Locate and identify every blood parasite.
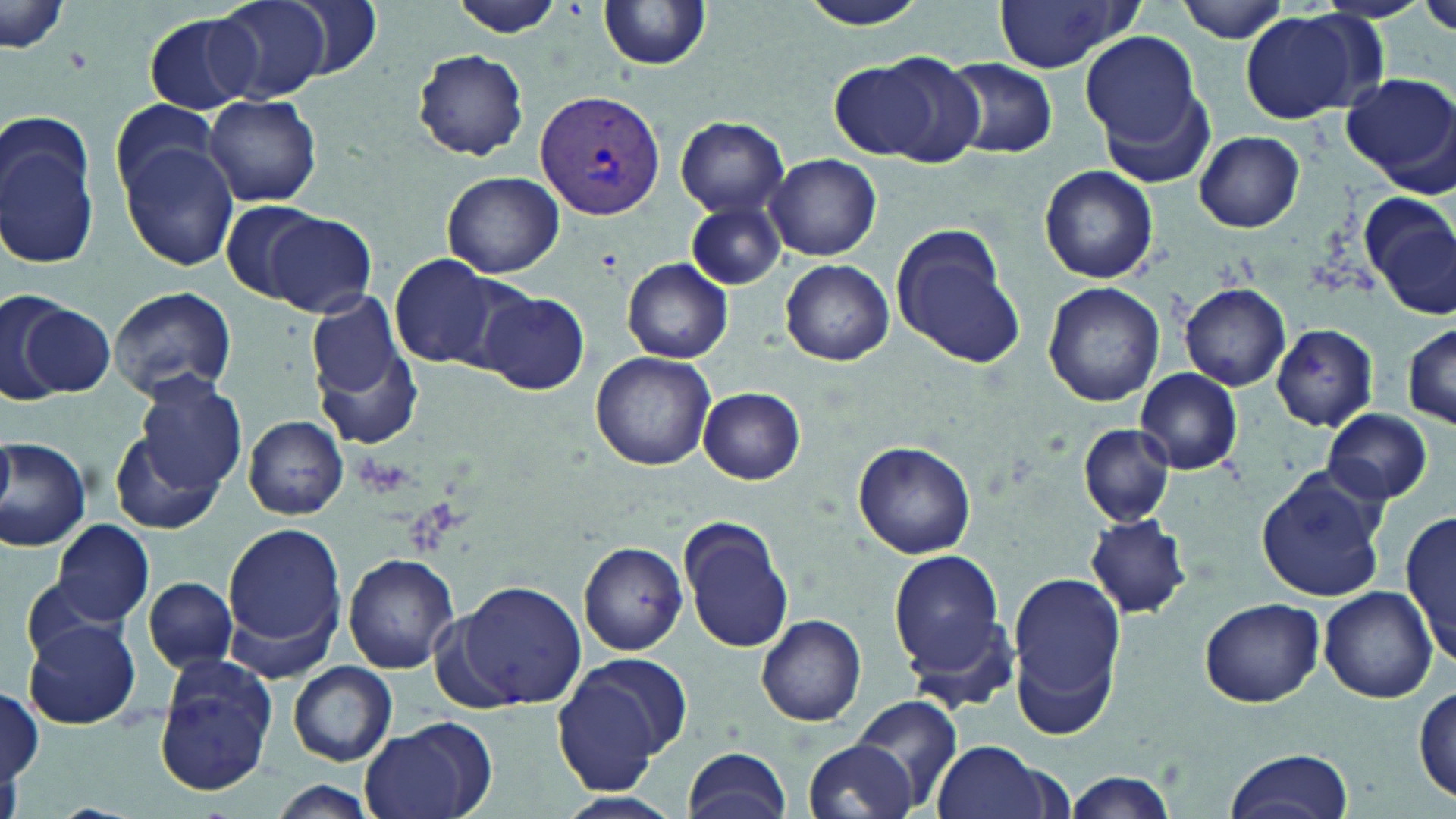
Approximate bounding boxes as named x1/y1/x2/y2 corners in pixels.
Plasmodium vivax-infected red blood cells: (x1=535, y1=89, x2=664, y2=219).
No Plasmodium falciparum, Plasmodium ovale, Plasmodium malariae, Babesia divergens, or Trypanosoma brucei observed.

slide-level diagnosis = Plasmodium vivax
stain = May-Grünwald-Giemsa
image size = 1456×819 pixels
magnification = 1000x
uninfected red blood cell locations = approximate bounding boxes as named x1/y1/x2/y2 corners in pixels: (x1=213, y1=0, x2=331, y2=102), (x1=287, y1=0, x2=387, y2=84), (x1=447, y1=0, x2=568, y2=36), (x1=798, y1=0, x2=930, y2=30), (x1=1173, y1=0, x2=1293, y2=43), (x1=1420, y1=0, x2=1456, y2=39), (x1=990, y1=1, x2=1139, y2=73), (x1=599, y1=2, x2=711, y2=72), (x1=1, y1=3, x2=71, y2=58), (x1=1239, y1=11, x2=1374, y2=125), (x1=143, y1=12, x2=261, y2=114), (x1=1080, y1=34, x2=1204, y2=156), (x1=414, y1=49, x2=530, y2=160), (x1=862, y1=52, x2=988, y2=165), (x1=944, y1=58, x2=1058, y2=159), (x1=832, y1=61, x2=935, y2=158), (x1=1096, y1=72, x2=1219, y2=190), (x1=1344, y1=73, x2=1456, y2=191), (x1=204, y1=95, x2=322, y2=206), (x1=110, y1=100, x2=221, y2=200), (x1=675, y1=115, x2=789, y2=215), (x1=0, y1=119, x2=100, y2=270), (x1=1194, y1=132, x2=1305, y2=232), (x1=120, y1=140, x2=239, y2=270), (x1=766, y1=153, x2=881, y2=260), (x1=1039, y1=166, x2=1158, y2=283), (x1=442, y1=171, x2=563, y2=278), (x1=1363, y1=196, x2=1456, y2=319), (x1=218, y1=199, x2=330, y2=304), (x1=685, y1=199, x2=785, y2=290), (x1=265, y1=213, x2=378, y2=317), (x1=888, y1=222, x2=1025, y2=371), (x1=390, y1=255, x2=500, y2=367), (x1=624, y1=258, x2=734, y2=362), (x1=782, y1=259, x2=894, y2=366), (x1=1042, y1=281, x2=1165, y2=407), (x1=1179, y1=283, x2=1291, y2=390), (x1=107, y1=286, x2=239, y2=403), (x1=1157, y1=288, x2=1276, y2=457), (x1=478, y1=290, x2=590, y2=395), (x1=1, y1=292, x2=104, y2=403), (x1=306, y1=294, x2=420, y2=448), (x1=1270, y1=322, x2=1380, y2=432), (x1=1404, y1=323, x2=1456, y2=429), (x1=591, y1=351, x2=717, y2=470), (x1=1135, y1=368, x2=1244, y2=475), (x1=130, y1=374, x2=249, y2=495), (x1=698, y1=387, x2=806, y2=485), (x1=1322, y1=408, x2=1434, y2=505), (x1=244, y1=416, x2=348, y2=519), (x1=1079, y1=424, x2=1174, y2=526), (x1=110, y1=433, x2=221, y2=535), (x1=1, y1=436, x2=93, y2=552), (x1=852, y1=441, x2=976, y2=560), (x1=1255, y1=470, x2=1388, y2=603), (x1=1401, y1=509, x2=1455, y2=662), (x1=1084, y1=513, x2=1191, y2=619), (x1=678, y1=516, x2=796, y2=653), (x1=51, y1=519, x2=155, y2=626), (x1=223, y1=521, x2=347, y2=660), (x1=578, y1=540, x2=688, y2=654), (x1=888, y1=547, x2=1015, y2=697), (x1=345, y1=553, x2=458, y2=674), (x1=1005, y1=567, x2=1127, y2=739), (x1=141, y1=577, x2=240, y2=674), (x1=453, y1=579, x2=586, y2=710), (x1=1318, y1=586, x2=1437, y2=702), (x1=1200, y1=598, x2=1324, y2=708), (x1=755, y1=614, x2=867, y2=727), (x1=23, y1=620, x2=142, y2=731), (x1=551, y1=655, x2=688, y2=793), (x1=154, y1=656, x2=280, y2=794), (x1=288, y1=660, x2=397, y2=766), (x1=1414, y1=687, x2=1455, y2=805), (x1=0, y1=689, x2=45, y2=784), (x1=845, y1=695, x2=966, y2=812), (x1=358, y1=716, x2=495, y2=819), (x1=804, y1=738, x2=918, y2=819), (x1=931, y1=739, x2=1061, y2=819), (x1=682, y1=745, x2=793, y2=819), (x1=1223, y1=748, x2=1353, y2=819), (x1=1061, y1=772, x2=1178, y2=818), (x1=269, y1=781, x2=381, y2=819), (x1=548, y1=792, x2=684, y2=819)
field of view = single
modality = light microscopy
preparation = thin blood film